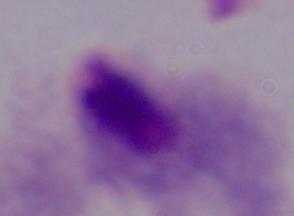

1000x magnification. A trichomonad is shown. Photomicrograph.